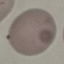
result = no malaria parasites seen
preparation = thin blood smear
image type = automatically extracted cell patch, resized to 64 × 64 pixels
capture = smartphone camera at the microscope eyepiece
stain = Giemsa